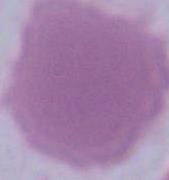
Summary:
  - Identification: erythrocyte
  - Modality: photomicrograph
  - Magnification: 1000x